Classify this cell by malaria status.
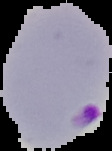
Parasitized.

image size = 112×151 pixels
image type = cell region segmented out of the field of view; surrounding area masked to black
preparation = thin blood film